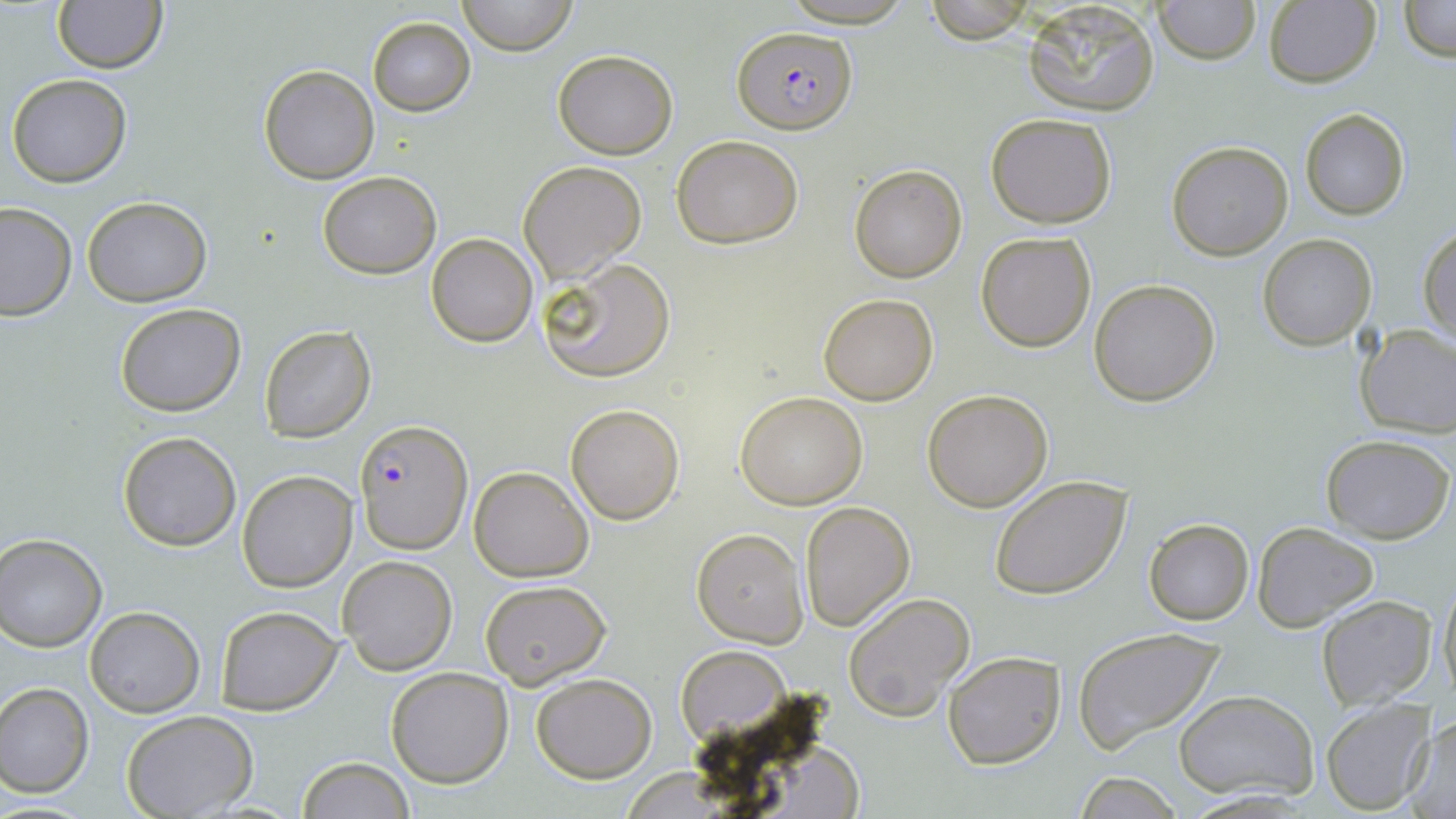

{
  "slide_level_diagnosis": "Plasmodium falciparum",
  "magnification": "1000x",
  "preparation": "thin blood film",
  "stain": "May-Grünwald-Giemsa",
  "image_size": "1456×819 pixels",
  "field_of_view": "one of a larger specimen",
  "plasmodium_falciparum_infected_red_blood_cell_locations": "approximate bounding boxes as (x1,y1)-(x2,y2) corner pairs in pixels: (734,24)-(857,134), (357,420)-(471,552)",
  "modality": "light microscopy",
  "uninfected_red_blood_cell_locations": "approximate bounding boxes as (x1,y1)-(x2,y2) corner pairs in pixels: (459,0)-(577,55), (777,0)-(918,27), (1153,0)-(1261,65), (1397,0)-(1456,63), (52,1)-(167,73), (922,1)-(1034,44), (1021,1)-(1161,118), (1261,2)-(1381,88), (367,16)-(475,116), (553,49)-(678,158), (260,65)-(379,183), (6,73)-(133,188), (1298,106)-(1411,221), (984,112)-(1118,229), (671,135)-(805,248), (1167,140)-(1295,261), (518,160)-(646,284), (847,164)-(967,283), (317,172)-(441,278), (83,197)-(211,306), (0,201)-(76,320), (1419,226)-(1455,344), (975,231)-(1098,353), (427,233)-(538,347), (1257,234)-(1376,350), (536,256)-(676,384), (1089,278)-(1220,406), (817,291)-(939,406), (115,303)-(247,417), (259,323)-(378,444), (1354,324)-(1456,440), (922,388)-(1054,512), (736,390)-(868,510), (565,403)-(685,524), (117,430)-(242,551), (1321,432)-(1455,544), (469,466)-(594,583), (237,469)-(358,592), (989,474)-(1132,599), (800,501)-(917,631), (1144,517)-(1254,624), (1251,521)-(1379,631), (691,529)-(809,648), (1,534)-(106,650), (337,555)-(457,675), (1437,574)-(1455,706), (478,578)-(613,690), (842,591)-(976,723), (1316,595)-(1435,709), (214,605)-(343,713), (84,606)-(205,716), (1070,627)-(1226,755), (675,645)-(790,744), (942,650)-(1066,769), (385,667)-(513,788), (530,673)-(655,782), (0,683)-(94,797), (1174,689)-(1321,802), (1320,702)-(1434,814), (121,711)-(259,819), (1409,714)-(1453,814), (296,757)-(417,818), (1073,769)-(1185,819)"
}